Assess this cell for malaria.
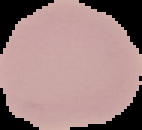

It is uninfected.

{
  "image_size": "142×130 pixels",
  "preparation": "thin blood film",
  "image_type": "cell region segmented out of the field of view; surrounding area masked to black"
}